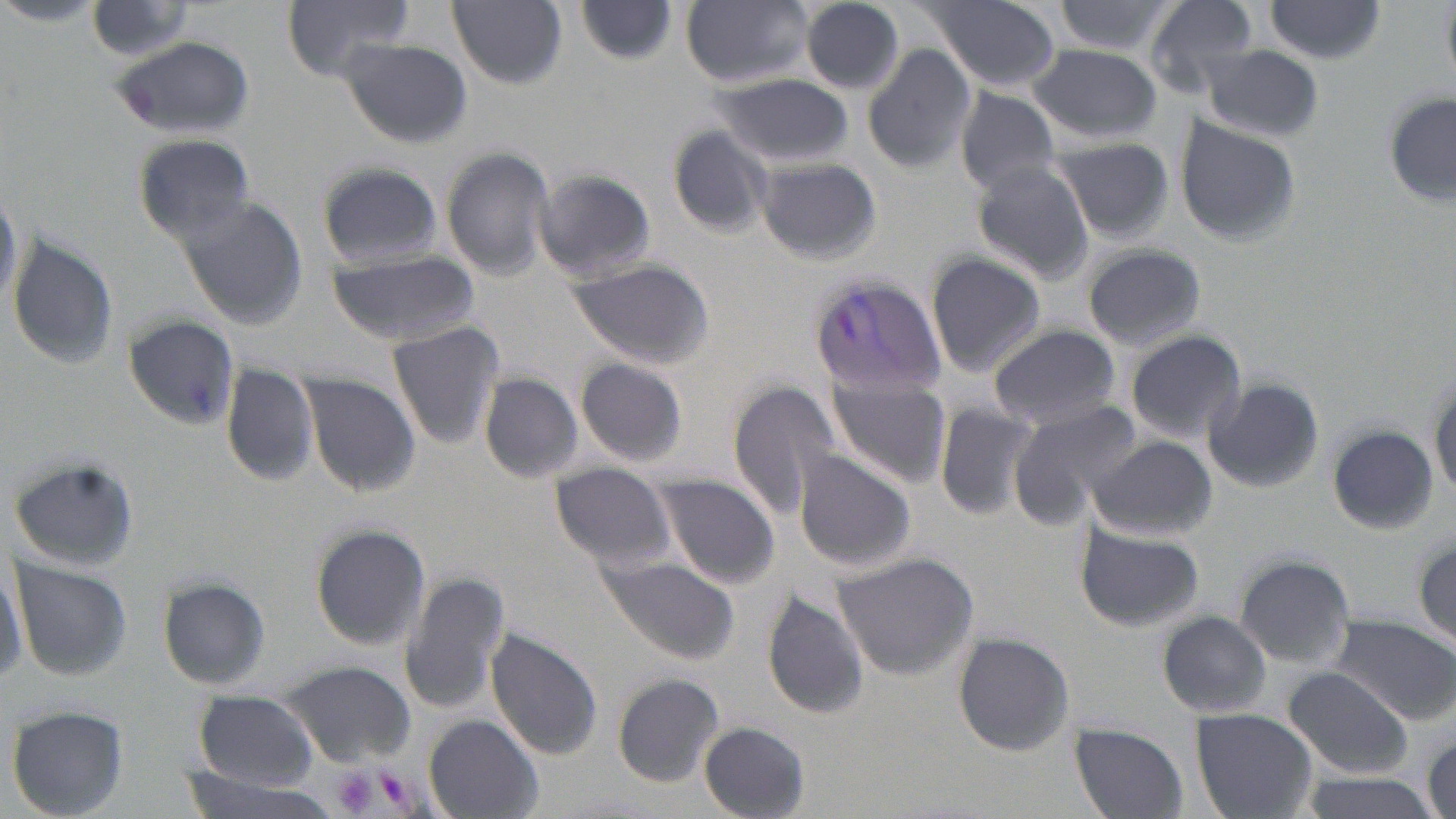 Approximate bounding boxes as (x1,y1)-(x2,y2) corner pairs in pixels. Uninfected red blood cell locations: (283,0)-(414,80), (447,0)-(568,89), (923,0)-(1065,92), (1051,0)-(1181,55), (1141,0)-(1262,99), (680,1)-(813,87), (799,1)-(906,95), (1262,1)-(1390,63), (0,2)-(100,27), (84,2)-(199,62), (575,3)-(680,66), (109,36)-(255,140), (336,38)-(473,149), (864,40)-(978,176), (1027,43)-(1161,142), (1202,46)-(1324,140), (710,76)-(855,167), (952,86)-(1065,195), (1385,95)-(1456,207), (1174,118)-(1301,248), (664,125)-(774,239), (134,133)-(256,240), (1047,139)-(1174,245), (439,146)-(554,282), (753,155)-(881,267), (968,160)-(1096,283), (317,162)-(441,269), (531,170)-(657,282), (0,186)-(21,314), (177,194)-(307,331), (10,237)-(117,369), (1083,244)-(1206,349), (326,247)-(479,347), (926,250)-(1047,378), (565,257)-(713,369), (127,318)-(242,432), (386,320)-(509,451), (988,324)-(1120,429), (1125,330)-(1247,444), (574,356)-(689,468), (220,362)-(321,489), (823,368)-(951,487), (478,372)-(585,486), (299,373)-(421,498), (1430,377)-(1455,503), (1204,379)-(1324,494), (729,381)-(845,515), (934,400)-(1037,521), (1007,400)-(1140,529), (696,406)-(827,553), (1329,426)-(1438,537), (1086,435)-(1215,540), (792,449)-(916,572), (5,458)-(140,570), (549,466)-(677,572), (650,473)-(779,588), (1072,520)-(1203,634), (310,524)-(431,649), (1414,536)-(1455,649), (832,551)-(979,680), (592,553)-(742,665), (0,554)-(26,691), (1233,554)-(1356,669), (11,559)-(133,680), (399,569)-(512,716), (158,578)-(272,690), (762,590)-(871,720), (1156,611)-(1274,718), (1325,614)-(1456,724), (482,627)-(604,762), (951,632)-(1075,755), (277,660)-(419,767), (1283,666)-(1414,779), (612,674)-(725,785), (189,692)-(321,793), (6,705)-(128,819), (1190,708)-(1318,819), (424,716)-(541,817), (698,723)-(810,817), (1069,724)-(1188,818), (168,769)-(345,819), (1287,771)-(1444,819). Platelet locations: (330,766)-(379,817), (377,771)-(409,807). Plasmodium vivax-infected red blood cell locations: (810,269)-(955,401). Slide-level diagnosis: Plasmodium vivax. Image is 1456×819 pixels. Captured at 1000x magnification. Thin blood smear. Light microscopy. May-Grünwald-Giemsa-stained preparation. Single field of view.